Classify this cell by malaria status.
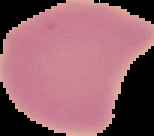

It is uninfected.

Summary:
  - Preparation: thin blood smear
  - Image size: 154×136 pixels
  - Image type: cell region segmented out of the field of view; surrounding area masked to black